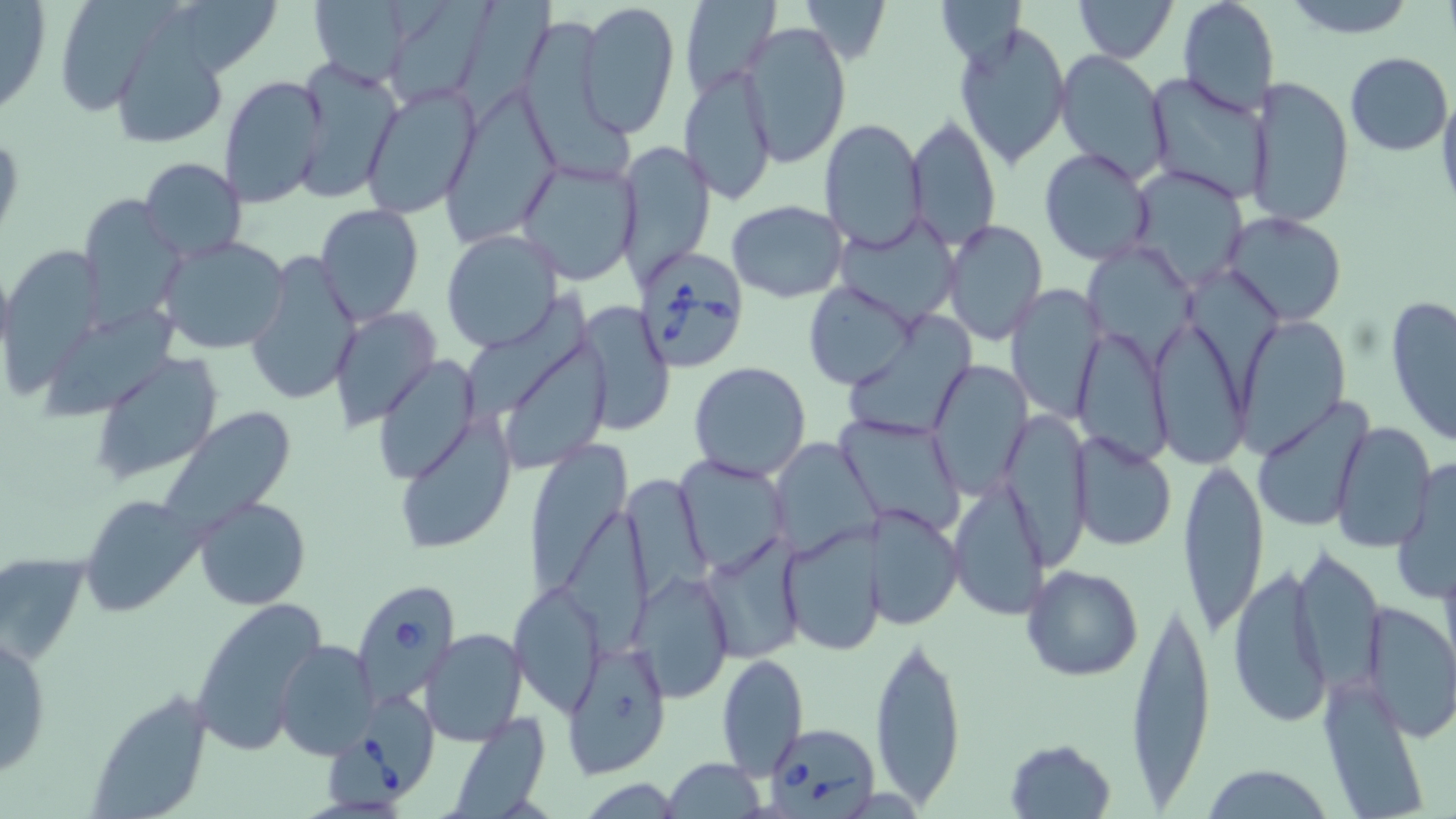
Summary:
  - Coordinate format: approximate bounding boxes as named x1/y1/x2/y2 corners in pixels
  - Uninfected red blood cell locations: (x1=0, y1=0, x2=51, y2=119), (x1=308, y1=0, x2=417, y2=88), (x1=578, y1=0, x2=681, y2=136), (x1=679, y1=0, x2=782, y2=102), (x1=798, y1=0, x2=890, y2=67), (x1=1072, y1=0, x2=1177, y2=62), (x1=1175, y1=0, x2=1280, y2=117), (x1=1278, y1=0, x2=1419, y2=38), (x1=393, y1=1, x2=505, y2=106), (x1=459, y1=1, x2=566, y2=110), (x1=934, y1=1, x2=1029, y2=63), (x1=62, y1=2, x2=181, y2=117), (x1=185, y1=2, x2=282, y2=74), (x1=954, y1=20, x2=1072, y2=169), (x1=738, y1=22, x2=853, y2=168), (x1=529, y1=23, x2=639, y2=181), (x1=113, y1=27, x2=229, y2=148), (x1=1054, y1=50, x2=1171, y2=183), (x1=1344, y1=52, x2=1452, y2=156), (x1=293, y1=60, x2=402, y2=202), (x1=680, y1=66, x2=778, y2=205), (x1=1145, y1=73, x2=1270, y2=204), (x1=219, y1=74, x2=329, y2=211), (x1=1248, y1=75, x2=1354, y2=230), (x1=362, y1=83, x2=481, y2=219), (x1=1436, y1=86, x2=1456, y2=217), (x1=444, y1=95, x2=560, y2=241), (x1=908, y1=114, x2=1003, y2=249), (x1=819, y1=118, x2=928, y2=252), (x1=617, y1=140, x2=717, y2=288), (x1=1038, y1=147, x2=1155, y2=266), (x1=138, y1=157, x2=247, y2=263), (x1=514, y1=157, x2=641, y2=286), (x1=1125, y1=163, x2=1248, y2=288), (x1=78, y1=198, x2=187, y2=330), (x1=727, y1=200, x2=848, y2=303), (x1=315, y1=203, x2=424, y2=327), (x1=1221, y1=211, x2=1347, y2=326), (x1=836, y1=214, x2=960, y2=327), (x1=940, y1=218, x2=1047, y2=345), (x1=440, y1=230, x2=563, y2=352), (x1=156, y1=236, x2=293, y2=355), (x1=1087, y1=244, x2=1193, y2=369), (x1=8, y1=246, x2=105, y2=394), (x1=245, y1=247, x2=363, y2=407), (x1=1189, y1=264, x2=1281, y2=403), (x1=1007, y1=281, x2=1105, y2=423), (x1=804, y1=283, x2=915, y2=389), (x1=466, y1=290, x2=588, y2=422), (x1=1384, y1=294, x2=1456, y2=450), (x1=580, y1=303, x2=675, y2=435), (x1=42, y1=305, x2=185, y2=416), (x1=331, y1=307, x2=441, y2=432), (x1=847, y1=308, x2=976, y2=434), (x1=1148, y1=315, x2=1250, y2=468), (x1=1233, y1=318, x2=1350, y2=457), (x1=1074, y1=321, x2=1174, y2=465), (x1=511, y1=341, x2=614, y2=472), (x1=90, y1=354, x2=223, y2=486), (x1=374, y1=355, x2=480, y2=486), (x1=924, y1=358, x2=1032, y2=499), (x1=687, y1=362, x2=813, y2=483), (x1=1249, y1=399, x2=1374, y2=533), (x1=156, y1=407, x2=300, y2=540), (x1=835, y1=412, x2=966, y2=536), (x1=1001, y1=412, x2=1094, y2=568), (x1=394, y1=413, x2=518, y2=556), (x1=1330, y1=419, x2=1437, y2=553), (x1=1069, y1=432, x2=1178, y2=552), (x1=520, y1=436, x2=630, y2=600), (x1=774, y1=438, x2=880, y2=561), (x1=1391, y1=454, x2=1456, y2=605), (x1=1176, y1=455, x2=1270, y2=639), (x1=674, y1=456, x2=791, y2=574), (x1=620, y1=472, x2=713, y2=605), (x1=949, y1=477, x2=1049, y2=621), (x1=79, y1=494, x2=199, y2=616), (x1=192, y1=495, x2=311, y2=610), (x1=866, y1=503, x2=963, y2=631), (x1=565, y1=504, x2=652, y2=664), (x1=778, y1=523, x2=884, y2=658), (x1=701, y1=537, x2=807, y2=665), (x1=1291, y1=543, x2=1388, y2=694), (x1=1, y1=554, x2=88, y2=668), (x1=1227, y1=561, x2=1335, y2=730), (x1=1022, y1=564, x2=1143, y2=682), (x1=633, y1=571, x2=735, y2=701), (x1=507, y1=581, x2=605, y2=717), (x1=189, y1=594, x2=330, y2=753), (x1=1125, y1=595, x2=1214, y2=807), (x1=1360, y1=601, x2=1456, y2=740), (x1=422, y1=629, x2=528, y2=745), (x1=869, y1=630, x2=968, y2=806), (x1=0, y1=631, x2=53, y2=781), (x1=274, y1=638, x2=380, y2=760), (x1=558, y1=642, x2=674, y2=779), (x1=716, y1=651, x2=808, y2=777), (x1=1319, y1=679, x2=1427, y2=815), (x1=85, y1=688, x2=217, y2=818), (x1=446, y1=715, x2=553, y2=818), (x1=1002, y1=737, x2=1118, y2=818), (x1=664, y1=757, x2=766, y2=818), (x1=1195, y1=765, x2=1337, y2=818), (x1=575, y1=779, x2=686, y2=815)
  - Babesia divergens-infected red blood cell locations: (x1=633, y1=248, x2=755, y2=376), (x1=352, y1=578, x2=460, y2=704), (x1=329, y1=695, x2=440, y2=809), (x1=762, y1=722, x2=882, y2=818)
  - Slide-level diagnosis: Babesia divergens
  - Modality: optical microscopy
  - Preparation: thin blood smear
  - Field of view: one of a larger specimen
  - Magnification: 1000x
  - Stain: May-Grünwald-Giemsa
  - Image size: 1456×819 pixels